Locate every P. falciparum parasite and identify its life-cycle stage.
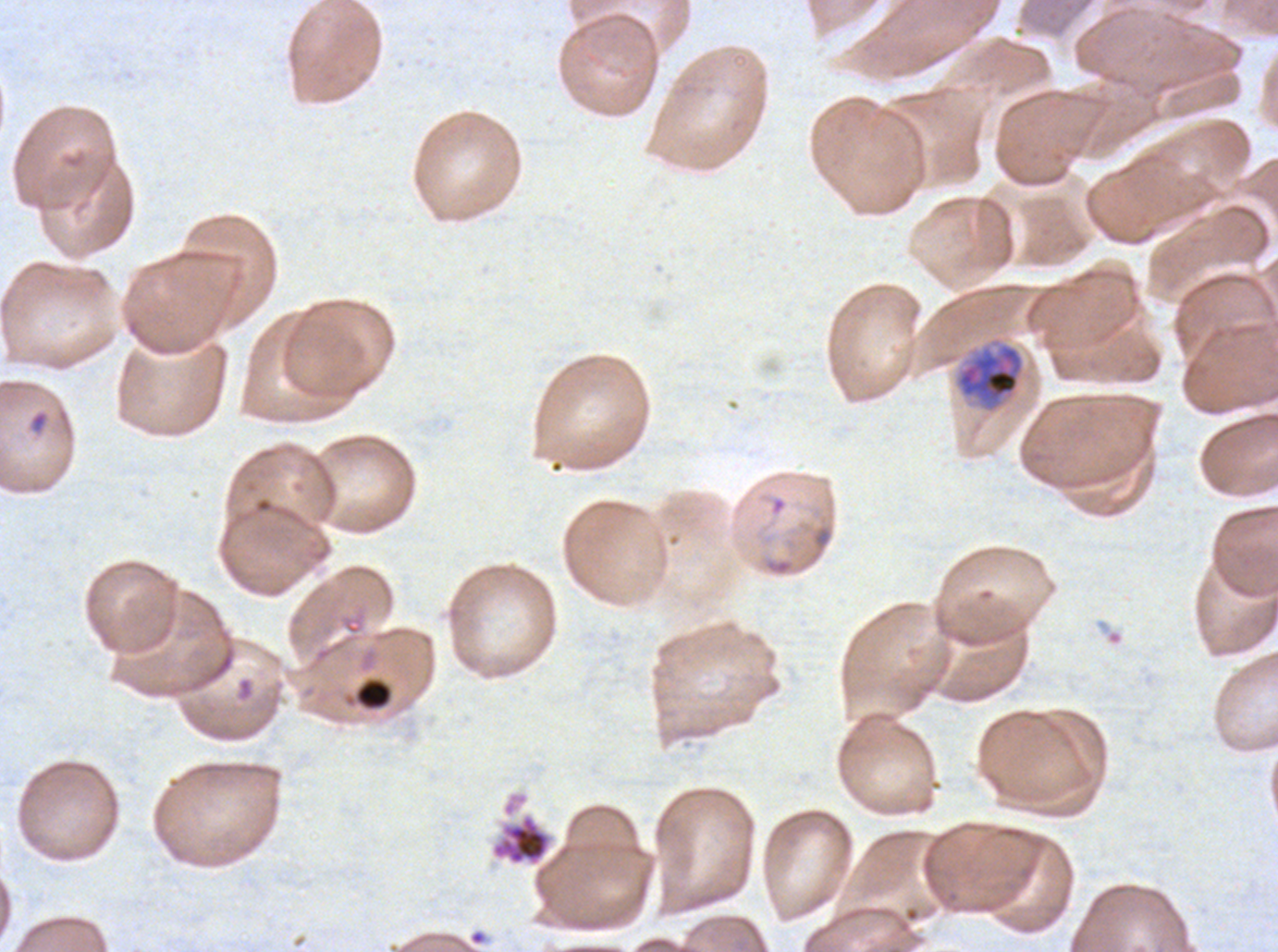
Approximate bounding boxes as (x1, y1, x2, y2) in pixels.
Rings: (29, 409, 50, 435).
Early schizonts: (955, 342, 1025, 412).
Segmenters: (491, 813, 551, 866).
No late-ring/early-trophozoite forms, mid trophozoites, late trophozoites, late schizonts, or gametocytes observed.

Debris locations: (355, 678, 392, 710). Thin blood film. Image is 1278×952 pixels. Life-cycle stages observed: ring, early schizont, segmenter. Ex-vivo P. falciparum culture from a patient in The Gambia, grown for 24 to 48 hours. A sub-image separated from a larger composite. Giemsa-stained preparation.